Assess this cell for malaria.
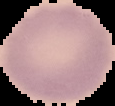

It is uninfected.

image size = 115×106 pixels
preparation = thin blood film
image type = segmented cell region on a black background